State which cell type is depicted.
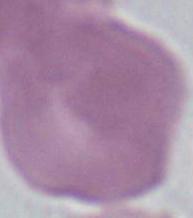
This is an erythrocyte.

Micrograph. Captured at 1000x magnification.